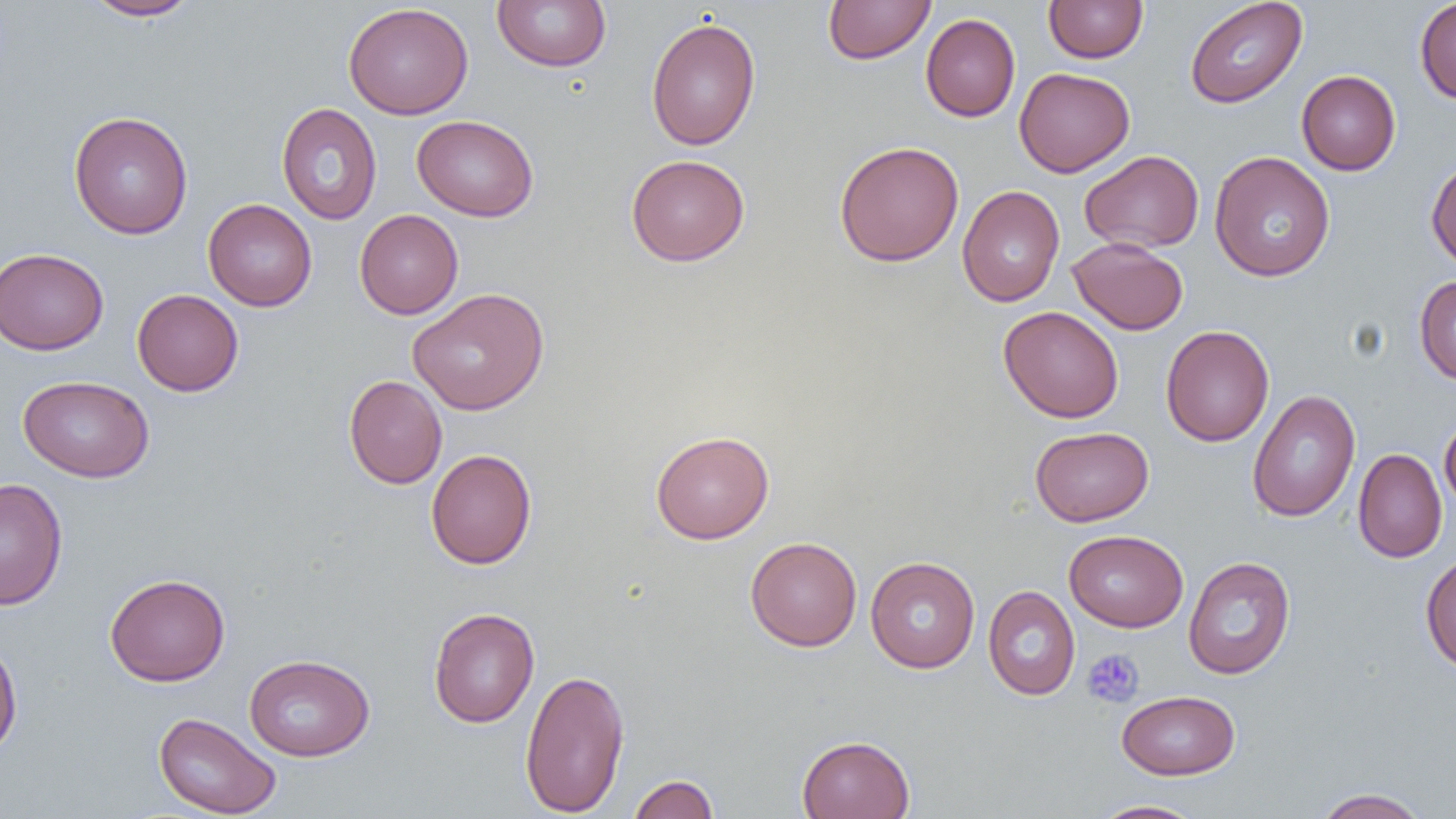

slide_level_diagnosis: negative for blood parasites
magnification: 1000x
uninfected_red_blood_cell_locations: 'approximate bounding boxes as named x1/y1/x2/y2 corners in pixels: (x1=83, y1=0, x2=200, y2=21), (x1=492, y1=0, x2=612, y2=72), (x1=822, y1=0, x2=935, y2=65), (x1=1043, y1=0, x2=1148, y2=63), (x1=1185, y1=0, x2=1307, y2=108), (x1=1414, y1=0, x2=1456, y2=104), (x1=343, y1=2, x2=473, y2=120), (x1=920, y1=13, x2=1021, y2=122), (x1=645, y1=16, x2=761, y2=151), (x1=1014, y1=67, x2=1135, y2=177), (x1=1296, y1=70, x2=1401, y2=175), (x1=276, y1=102, x2=382, y2=224), (x1=68, y1=111, x2=193, y2=239), (x1=412, y1=115, x2=539, y2=221), (x1=834, y1=140, x2=964, y2=267), (x1=1080, y1=150, x2=1204, y2=253), (x1=1209, y1=151, x2=1335, y2=282), (x1=626, y1=154, x2=750, y2=266), (x1=1426, y1=157, x2=1456, y2=271), (x1=957, y1=186, x2=1065, y2=307), (x1=203, y1=198, x2=317, y2=311), (x1=354, y1=209, x2=463, y2=319), (x1=1067, y1=237, x2=1189, y2=335), (x1=0, y1=247, x2=109, y2=355), (x1=1414, y1=274, x2=1456, y2=385), (x1=407, y1=288, x2=549, y2=415), (x1=132, y1=289, x2=244, y2=396), (x1=998, y1=305, x2=1124, y2=423), (x1=1160, y1=324, x2=1274, y2=446), (x1=18, y1=375, x2=155, y2=482), (x1=344, y1=375, x2=447, y2=489), (x1=1247, y1=390, x2=1361, y2=522), (x1=1439, y1=414, x2=1456, y2=513), (x1=1029, y1=426, x2=1153, y2=527), (x1=650, y1=430, x2=774, y2=544), (x1=1353, y1=448, x2=1447, y2=563), (x1=426, y1=449, x2=537, y2=570), (x1=0, y1=477, x2=68, y2=610), (x1=1064, y1=529, x2=1188, y2=631), (x1=745, y1=536, x2=862, y2=651), (x1=1420, y1=552, x2=1456, y2=673), (x1=865, y1=556, x2=980, y2=673), (x1=1183, y1=556, x2=1296, y2=680), (x1=104, y1=573, x2=230, y2=686), (x1=983, y1=585, x2=1080, y2=701), (x1=427, y1=607, x2=540, y2=728), (x1=0, y1=635, x2=22, y2=758), (x1=244, y1=653, x2=375, y2=761), (x1=519, y1=668, x2=631, y2=817), (x1=1116, y1=690, x2=1240, y2=780), (x1=154, y1=711, x2=281, y2=818), (x1=797, y1=734, x2=915, y2=818), (x1=627, y1=774, x2=719, y2=819), (x1=1312, y1=787, x2=1430, y2=818), (x1=1089, y1=799, x2=1207, y2=819)'
field_of_view: single
preparation: thin blood film
platelet_locations: 'approximate bounding boxes as named x1/y1/x2/y2 corners in pixels: (x1=1082, y1=649, x2=1144, y2=707)'
modality: light microscopy
image_size: 1456×819 pixels